Outline each Trypanosoma brucei.
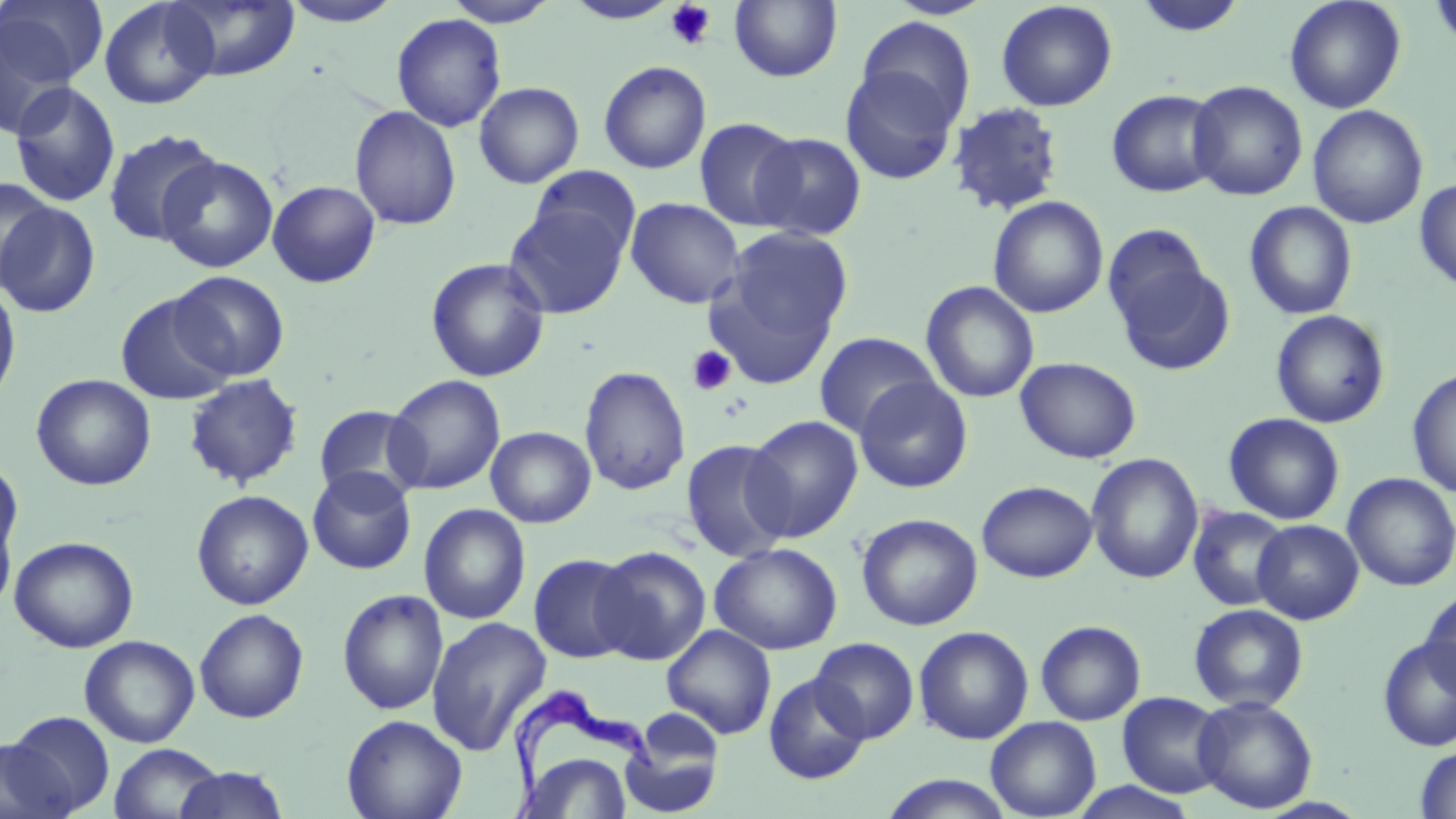

Approximate bounding boxes as [x1, y1, x2, y2] in pixels.
Trypanosoma brucei: [504, 690, 660, 815].

Summary:
  - Uninfected red blood cell locations: [167, 0, 301, 82], [279, 0, 406, 27], [443, 0, 558, 27], [564, 0, 681, 24], [729, 0, 842, 83], [1132, 0, 1248, 39], [1284, 0, 1406, 114], [1427, 0, 1456, 52], [1, 1, 107, 88], [99, 1, 219, 109], [996, 1, 1117, 111], [392, 13, 506, 132], [856, 16, 976, 132], [0, 19, 77, 139], [598, 60, 712, 174], [839, 64, 962, 185], [1187, 80, 1308, 201], [473, 81, 584, 188], [9, 82, 122, 208], [1106, 89, 1224, 197], [947, 101, 1066, 216], [1308, 104, 1428, 229], [350, 105, 461, 231], [694, 117, 804, 231], [103, 128, 222, 246], [750, 132, 867, 241], [157, 155, 278, 273], [527, 166, 642, 261], [0, 178, 57, 293], [1414, 178, 1456, 291], [267, 180, 381, 288], [988, 196, 1108, 318], [625, 197, 745, 309], [503, 200, 631, 319], [1244, 201, 1358, 320], [1, 202, 102, 318], [714, 226, 853, 363], [1108, 243, 1235, 375], [425, 257, 551, 383], [172, 270, 290, 381], [0, 280, 22, 410], [920, 280, 1039, 403], [115, 292, 236, 405], [1270, 309, 1391, 429], [814, 332, 939, 438], [1016, 356, 1142, 464], [579, 365, 691, 496], [1407, 367, 1456, 498], [30, 374, 156, 490], [184, 374, 304, 489], [385, 374, 506, 494], [854, 376, 973, 493], [313, 404, 425, 503], [1224, 413, 1345, 525], [743, 414, 863, 542], [486, 426, 596, 528], [681, 439, 793, 562], [1086, 453, 1204, 583], [0, 457, 23, 565], [307, 466, 416, 575], [1342, 473, 1456, 592], [976, 480, 1097, 583], [191, 489, 313, 610], [419, 503, 531, 624], [1187, 506, 1291, 612], [0, 507, 17, 618], [856, 513, 983, 631], [1252, 519, 1364, 624], [9, 535, 139, 653], [709, 542, 843, 655], [592, 546, 711, 665], [529, 554, 640, 663], [1420, 587, 1456, 698], [337, 588, 449, 715], [1189, 603, 1309, 712], [194, 608, 309, 723], [426, 616, 552, 756], [1035, 619, 1146, 725], [662, 625, 777, 739], [913, 625, 1034, 744], [1377, 634, 1456, 752], [79, 635, 200, 747], [810, 637, 920, 743], [763, 672, 871, 785], [1117, 692, 1229, 798], [1192, 695, 1318, 814], [620, 709, 726, 818], [5, 710, 116, 815], [341, 714, 467, 819], [985, 717, 1101, 818], [0, 737, 72, 819], [108, 743, 226, 819], [1414, 744, 1456, 819], [519, 753, 634, 818], [173, 766, 291, 818], [878, 774, 1017, 818], [1068, 781, 1201, 819]
  - Platelet locations: [665, 1, 717, 50], [687, 346, 736, 396]
  - Slide-level diagnosis: Trypanosoma brucei
  - Modality: light microscopy
  - Image size: 1456×819 pixels
  - Preparation: thin blood smear
  - Stain: May-Grünwald-Giemsa
  - Magnification: 1000x
  - Field of view: one of a larger specimen